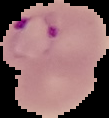

preparation = thin blood smear
image size = 109×118 pixels
image type = cell region segmented out of the field of view; surrounding area masked to black
malaria status = parasitized